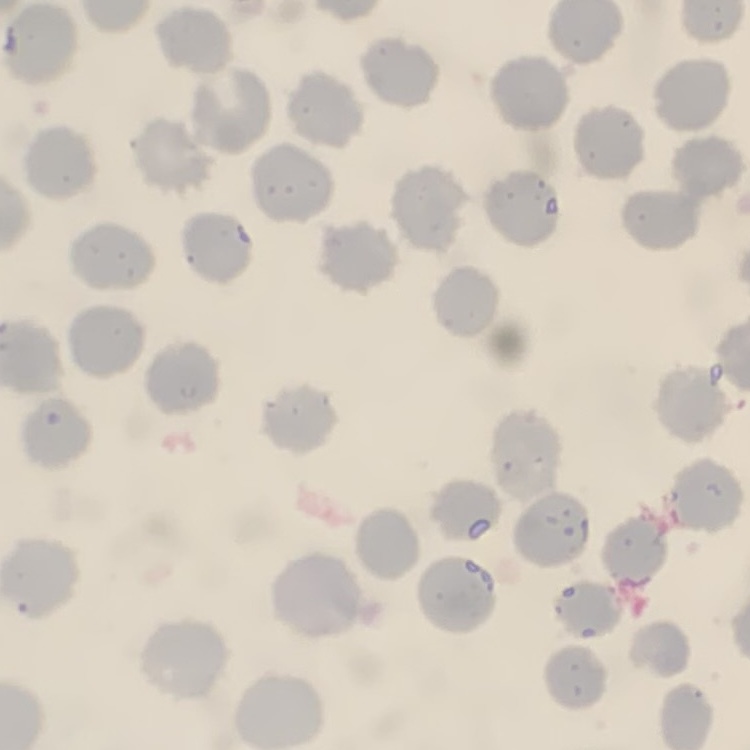
Summary:
  - Red blood cell morphology: no rouleaux formation
  - Preparation: thin blood smear
  - Image type: one tile cut from a larger photomicrograph
  - Stain: Field's or Giemsa